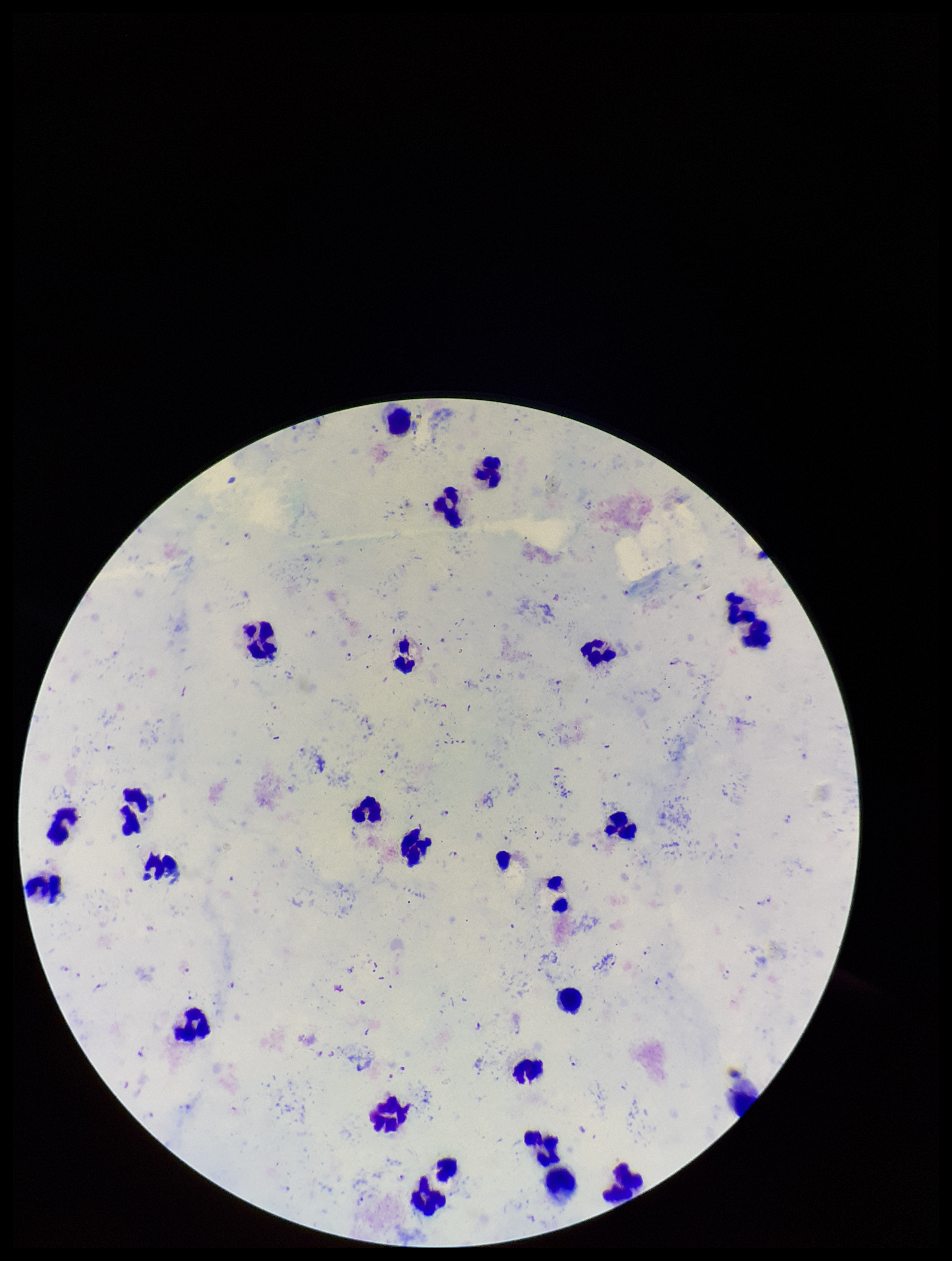
capture = smartphone photograph through the microscope eyepiece
Plasmodium parasites = seen
preparation = thick smear
species reported for this patient = Plasmodium falciparum
field of view = single
parasite count = 38
patient malaria status = positive
image size = 952×1261 pixels
stain = Giemsa
leukocyte count = 29